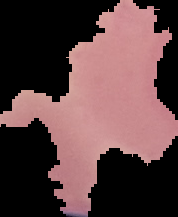 Malaria status: parasitized. Image is 178×217 pixels. The area outside the segmented cell region is set to black. From a thin blood smear.